Assess this cell for malaria.
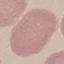
Uninfected.

Giemsa-stained preparation. Photographed with a smartphone camera at the microscope eyepiece. Cell patch, automatically extracted from a larger field of view and resized to 64 × 64 pixels. Thin blood smear.